Assess this cell for malaria.
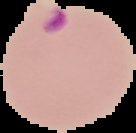

Parasitized.

preparation = thin blood smear
image type = cell region segmented out of the field of view; surrounding area masked to black
image size = 136×133 pixels